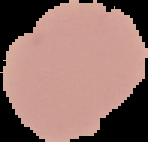
From a thin blood smear. Result: no malaria parasites detected. Image is 148×142 pixels. The area outside the segmented cell region is set to black.